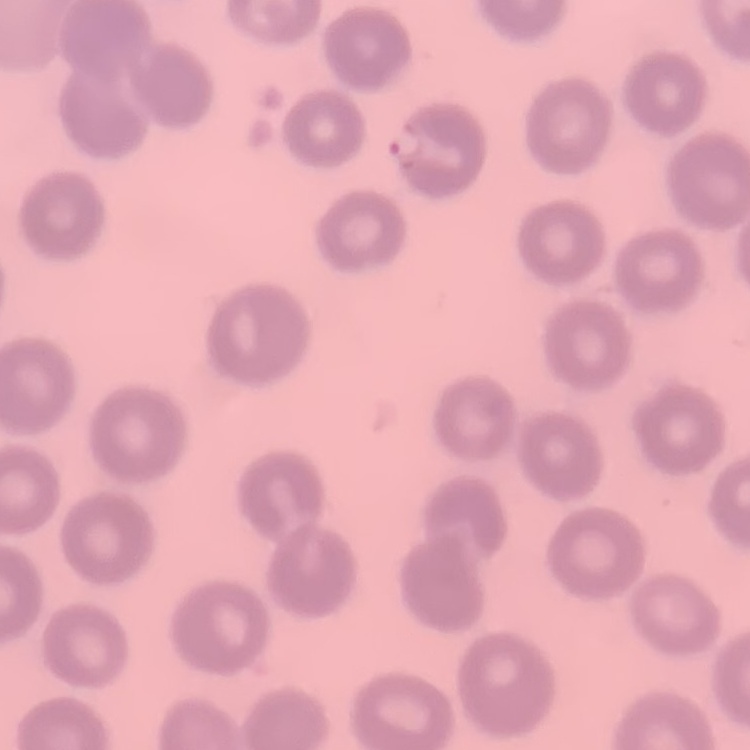

Summary:
  - Red blood cell morphology: no rouleaux formation
  - Stain: Field's or Giemsa
  - Image type: one tile cut from a larger photomicrograph
  - Preparation: thin blood smear